Classify this cell by malaria status.
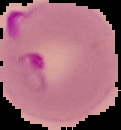
It is parasitized.

image size = 121×130 pixels
preparation = thin blood smear
image type = segmented cell region with the area outside set to black